Assess this cell for malaria.
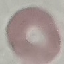
It is uninfected.

Photographed with a smartphone camera at the microscope eyepiece. Automatically extracted cell patch, resized to 64 × 64 pixels. Thin smear of blood. Giemsa-stained preparation.